Assess this cell for malaria.
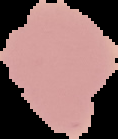

Uninfected.

{
  "image_type": "cell region segmented out of the field of view; surrounding area masked to black",
  "image_size": "118×139 pixels",
  "preparation": "thin blood film"
}